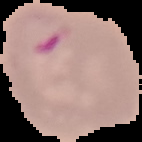
image_type: segmented cell region with the area outside set to black
preparation: thin blood film
image_size: 142×142 pixels
result: malaria parasites identified